Give the position of every malaria parasite.
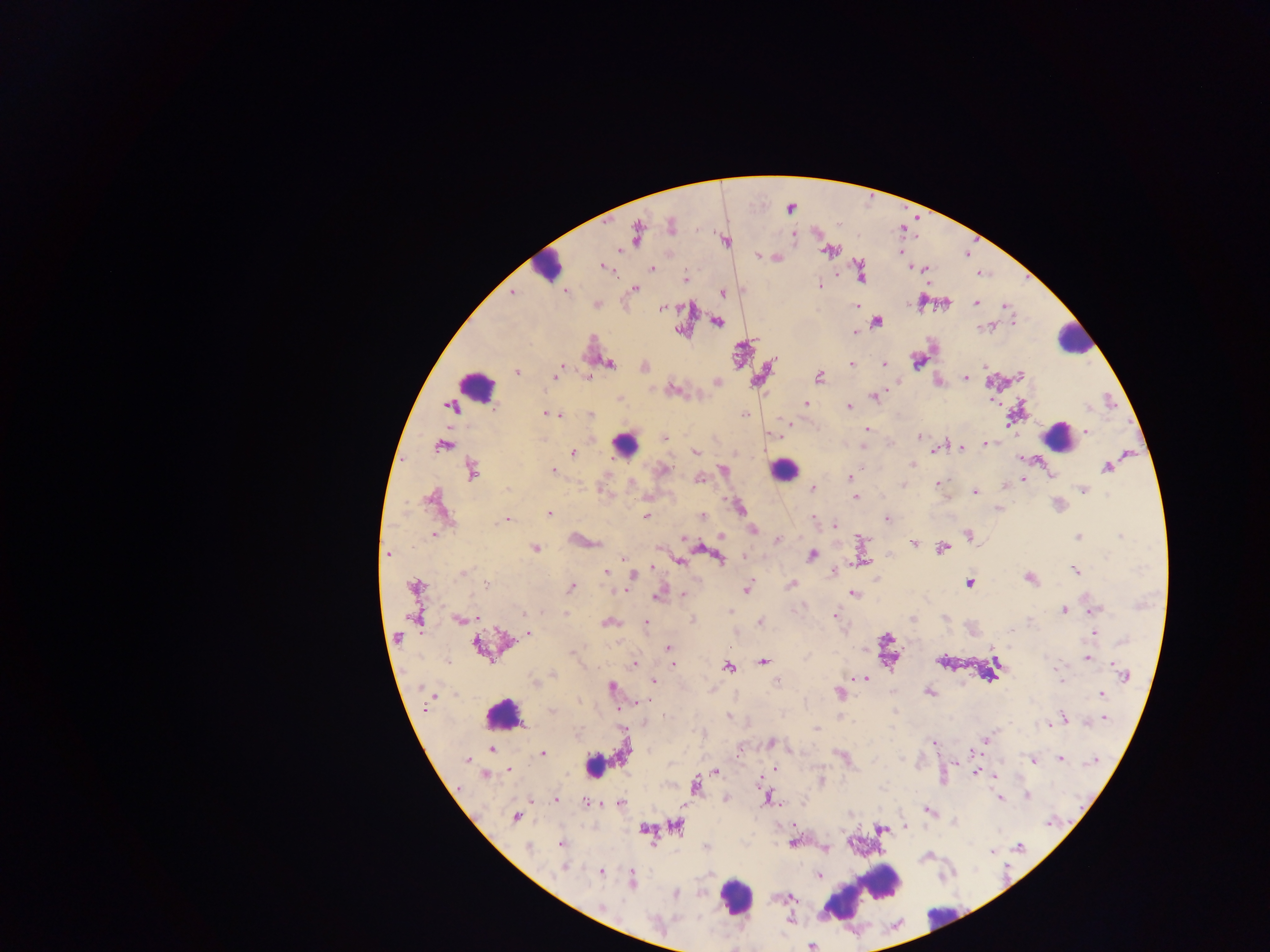
Approximate centers as (x, y) in pixels.
Malaria parasites: (670, 225), (637, 233), (725, 241), (827, 252), (758, 257), (602, 267), (925, 268), (651, 269), (861, 273), (684, 279), (819, 285), (635, 288), (566, 292), (512, 293), (722, 293), (976, 302), (1005, 305), (856, 306), (662, 308), (877, 321), (1013, 321), (718, 323), (984, 327), (854, 333), (776, 359), (917, 362), (609, 363), (851, 364), (884, 364), (560, 367), (645, 367), (517, 371), (557, 374), (1021, 374), (965, 377), (819, 378), (717, 383), (673, 388), (875, 397), (620, 398), (806, 403), (849, 406), (451, 407), (548, 413), (745, 414), (557, 415), (609, 417), (787, 423), (867, 430), (1087, 432), (665, 437), (919, 437), (986, 443), (441, 446), (862, 447), (962, 448), (934, 451), (695, 452), (573, 453), (912, 464), (1107, 467), (664, 469), (723, 469), (860, 469), (553, 470), (472, 472), (851, 477), (700, 479), (1023, 479), (812, 484), (937, 484), (903, 485), (1083, 490), (975, 492), (855, 496), (738, 506), (999, 509), (549, 513), (646, 515), (702, 516), (813, 517), (887, 519), (507, 520), (835, 525), (752, 529), (968, 534), (433, 535), (721, 536), (1120, 536), (1078, 537), (684, 539), (777, 540), (915, 543), (535, 548), (942, 548), (388, 554), (812, 555), (744, 556), (719, 558), (622, 559), (680, 561), (652, 567), (607, 571), (1077, 571), (463, 573), (633, 575), (1030, 578), (969, 583), (485, 585), (791, 585), (415, 586), (571, 588), (746, 589), (622, 591), (853, 594), (683, 595), (656, 598), (1064, 610), (1094, 610), (542, 612), (730, 612), (566, 613), (523, 614), (835, 615), (478, 618), (945, 618), (912, 619), (459, 620), (693, 620), (1029, 621), (646, 622), (609, 623), (761, 623), (529, 633), (1094, 633), (1122, 641), (478, 646), (667, 648), (993, 649), (572, 652), (1087, 658), (670, 661), (762, 661), (673, 664), (634, 665), (729, 667), (1057, 669), (1120, 671), (553, 675), (1124, 675), (1058, 676), (856, 678), (865, 679), (1061, 680), (653, 681), (534, 682), (776, 682), (612, 687), (838, 692), (929, 692), (1101, 693), (579, 701), (646, 701), (427, 709), (618, 709), (552, 711), (728, 717), (1064, 717), (1105, 719), (1049, 725), (816, 728), (987, 738), (771, 743), (933, 743), (492, 750), (976, 752), (542, 754), (841, 757), (1061, 759), (467, 760), (1032, 760), (1093, 762), (509, 769), (775, 769), (716, 771), (975, 773), (995, 775), (485, 776), (821, 780), (758, 781), (695, 787), (1028, 796), (767, 797), (725, 798), (1000, 798), (556, 800), (585, 802), (597, 803), (620, 803), (929, 810), (515, 817), (1048, 823), (678, 825), (904, 826), (644, 829), (881, 830), (793, 842), (561, 843), (527, 847), (705, 847), (1020, 847), (992, 851), (564, 867), (601, 871), (820, 875), (632, 879), (676, 894), (789, 898), (601, 906), (789, 919), (811, 947).
One object is labeled both malaria parasite and leukocyte by the source: (593, 766).

leukocyte locations = approximate centers as (x, y) in pixels: (546, 265), (1074, 338), (475, 386), (1059, 431), (627, 445), (783, 470), (504, 714), (866, 891), (735, 897), (943, 921)
capture = mobile-phone photograph through a microscope
field of view = single
image size = 1270×952 pixels
country = Ghana
preparation = thick blood smear